Comment on the morphology of the erythrocytes.
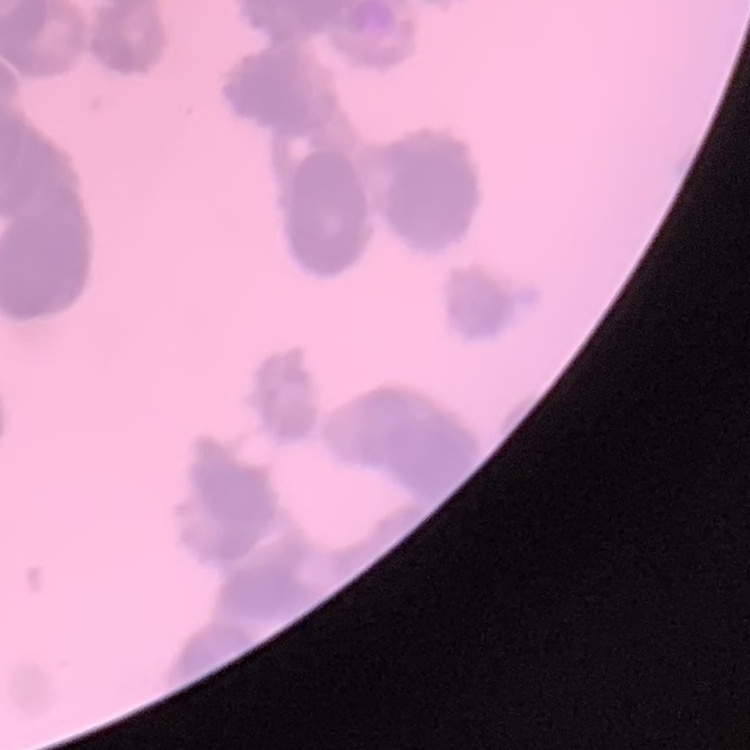
They show rouleaux formation.

{
  "preparation": "thin peripheral smear",
  "stain": "Field's or Giemsa",
  "image_type": "one tile cut from a larger photomicrograph"
}